Locate leukocytes (white blood cells).
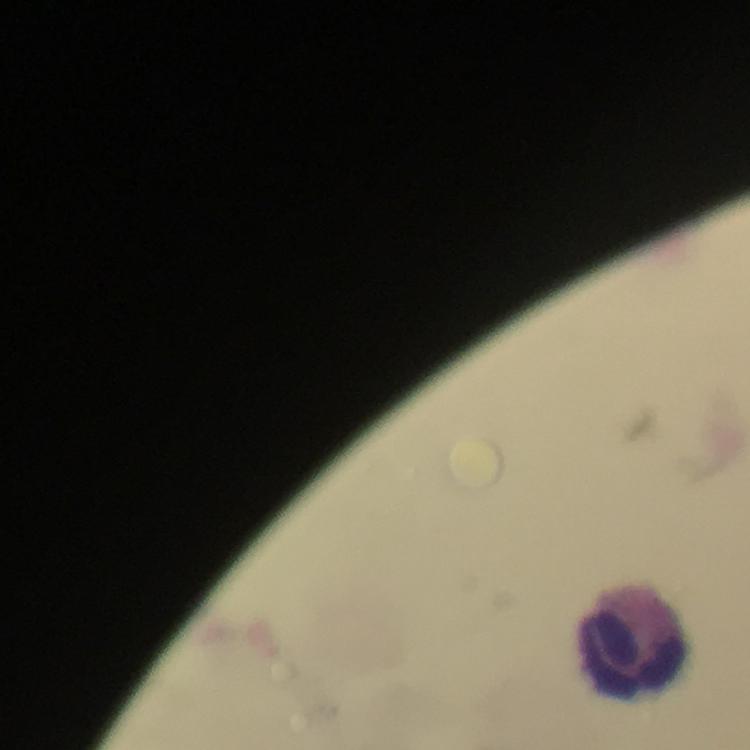
Approximate centers as [x, y] in pixels.
Leukocytes: [636, 640].

Cropped region of a single field of view. At 100x magnification. Thick blood smear. Malaria parasites: none seen. From a diagnostic examination for malaria. Giemsa-stained preparation. Image is 750×750 pixels. Smartphone photograph taken through a microscope. Immersion oil was used.